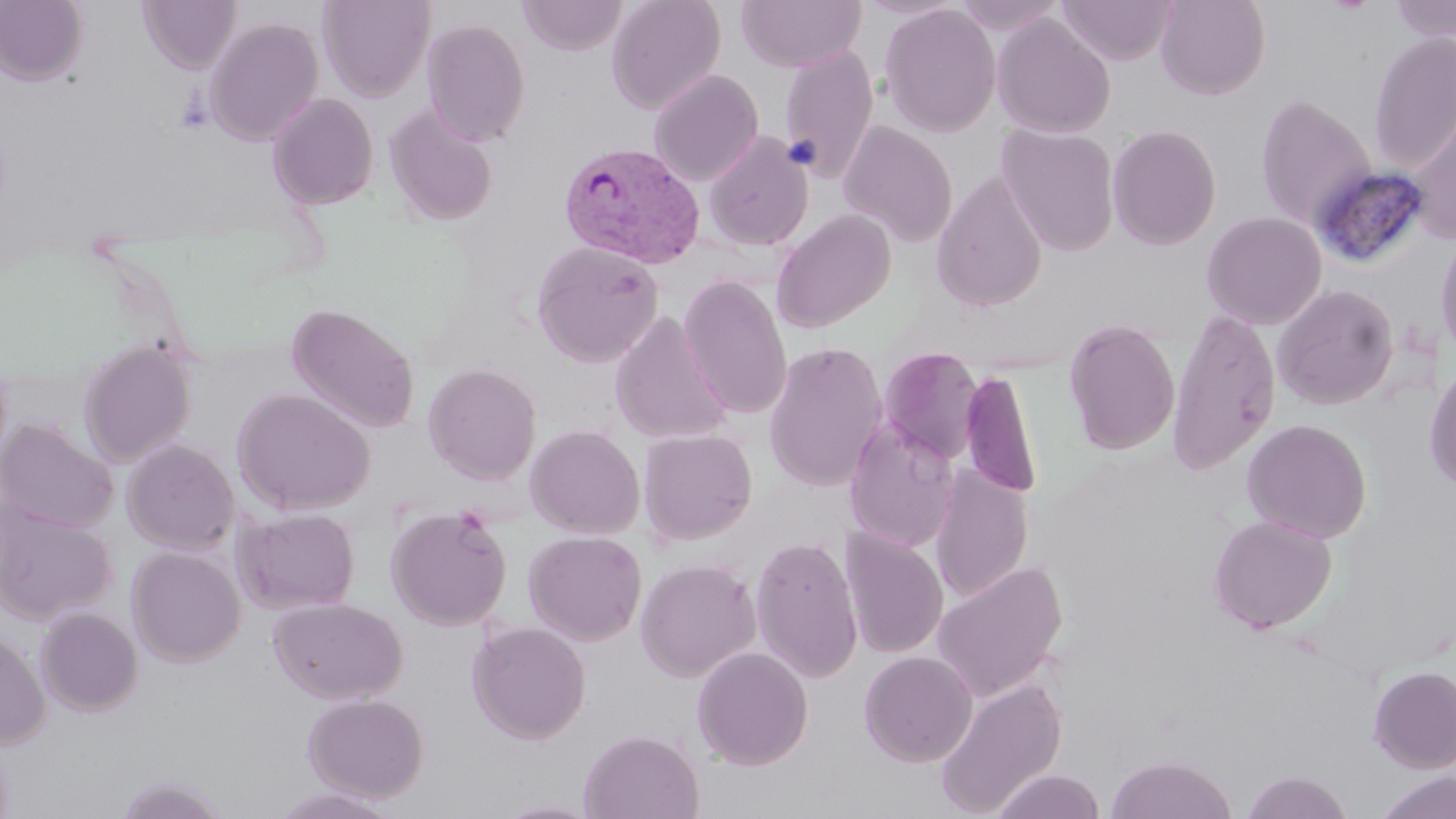

Approximate bounding boxes as (x1, y1, x2, y2) in pixels. Uninfected red blood cell locations: (0, 0, 89, 86), (137, 0, 241, 73), (317, 0, 435, 101), (517, 0, 628, 55), (606, 0, 726, 115), (736, 0, 866, 71), (1154, 0, 1271, 100), (1389, 0, 1456, 42), (1056, 1, 1177, 66), (880, 4, 1001, 137), (991, 13, 1115, 139), (204, 17, 324, 146), (422, 18, 531, 146), (1367, 32, 1456, 171), (779, 45, 879, 181), (648, 69, 764, 186), (1255, 92, 1376, 230), (266, 93, 379, 210), (385, 104, 499, 226), (1406, 109, 1456, 242), (838, 121, 958, 246), (997, 124, 1120, 255), (1106, 124, 1222, 250), (704, 133, 813, 252), (932, 172, 1048, 312), (772, 209, 896, 333), (1201, 211, 1327, 330), (1434, 225, 1456, 364), (531, 240, 664, 367), (678, 274, 793, 419), (1272, 285, 1398, 410), (287, 303, 420, 434), (1167, 308, 1281, 475), (610, 311, 732, 445), (1063, 318, 1181, 456), (78, 339, 196, 467), (763, 341, 888, 492), (878, 346, 985, 464), (1423, 358, 1456, 494), (423, 363, 541, 484), (960, 369, 1043, 499), (232, 388, 376, 516), (844, 417, 960, 553), (1242, 418, 1372, 543), (0, 420, 118, 533), (525, 424, 645, 539), (639, 428, 757, 545), (122, 439, 240, 554), (930, 466, 1034, 604), (0, 506, 117, 624), (386, 506, 512, 631), (232, 507, 360, 614), (1208, 514, 1337, 633), (841, 528, 948, 659), (523, 530, 647, 645), (750, 534, 863, 682), (127, 546, 246, 667), (635, 559, 761, 682), (932, 559, 1068, 704), (267, 596, 408, 704), (36, 606, 144, 715), (466, 621, 591, 744), (0, 627, 51, 750), (691, 645, 813, 770), (859, 650, 978, 767), (1368, 664, 1456, 773), (933, 676, 1068, 818), (303, 693, 429, 802), (579, 729, 704, 819), (1105, 754, 1237, 819), (991, 769, 1108, 819), (1241, 770, 1354, 818), (1376, 770, 1456, 819), (112, 775, 233, 818), (271, 785, 403, 818). Plasmodium vivax-infected red blood cell locations: (559, 140, 704, 268). Slide-level diagnosis: Plasmodium vivax. May-Grünwald-Giemsa-stained preparation. Image is 1456×819 pixels. Thin blood film. Single field of view. Light microscopy. 1000x magnification.